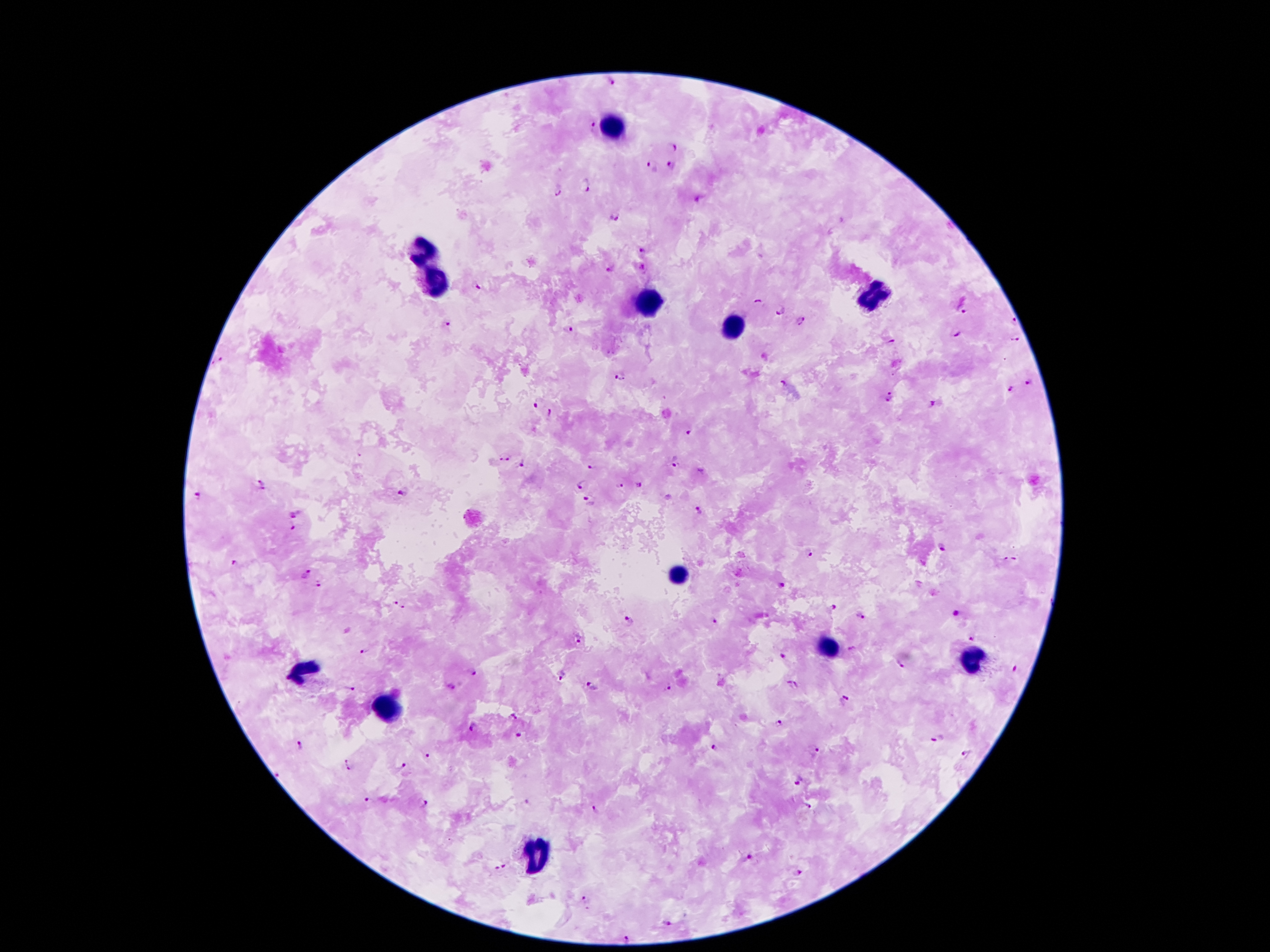

Approximate centers as (x, y) in pixels. Plasmodium parasite locations: (607, 82), (593, 124), (672, 145), (671, 165), (652, 166), (587, 186), (558, 189), (698, 202), (614, 217), (645, 250), (643, 266), (608, 268), (477, 285), (758, 301), (781, 309), (964, 311), (799, 321), (1013, 321), (449, 323), (570, 328), (956, 335), (1014, 339), (892, 342), (620, 377), (782, 380), (1030, 382), (1010, 389), (889, 397), (536, 402), (931, 405), (552, 412), (689, 432), (503, 459), (522, 464), (675, 465), (591, 466), (261, 482), (582, 485), (637, 485), (621, 486), (262, 489), (404, 491), (197, 495), (588, 501), (699, 512), (295, 514), (293, 527), (943, 547), (809, 552), (1010, 559), (234, 562), (304, 575), (319, 586), (780, 586), (394, 600), (403, 607), (833, 607), (956, 614), (860, 616), (713, 620), (631, 622), (972, 637), (578, 638), (852, 649), (366, 651), (783, 656), (900, 664), (1014, 668), (472, 673), (560, 676), (793, 686), (451, 687), (592, 687), (668, 687), (351, 690), (842, 702), (513, 717), (778, 723), (475, 727), (520, 737), (938, 739), (300, 745), (714, 748), (815, 752), (428, 755), (969, 755), (351, 764), (403, 767), (280, 773), (799, 781), (368, 800), (527, 801), (424, 804), (807, 806), (593, 810), (750, 858), (500, 868), (798, 871), (586, 897), (667, 921), (630, 937). Leukocyte locations: (614, 128), (422, 253), (437, 283), (874, 294), (644, 305), (732, 327), (676, 574), (825, 648), (969, 661), (304, 672), (387, 711), (530, 855). Giemsa-stained preparation. Smartphone photograph taken through the microscope eyepiece. Patient malaria status: positive for Plasmodium falciparum. Image is 1270×952 pixels. 100x magnification. One field from this slide. Thick blood smear.